Name the parasite shown.
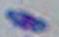
Toxoplasma gondii.

{
  "modality": "micrograph",
  "magnification": "1000x"
}